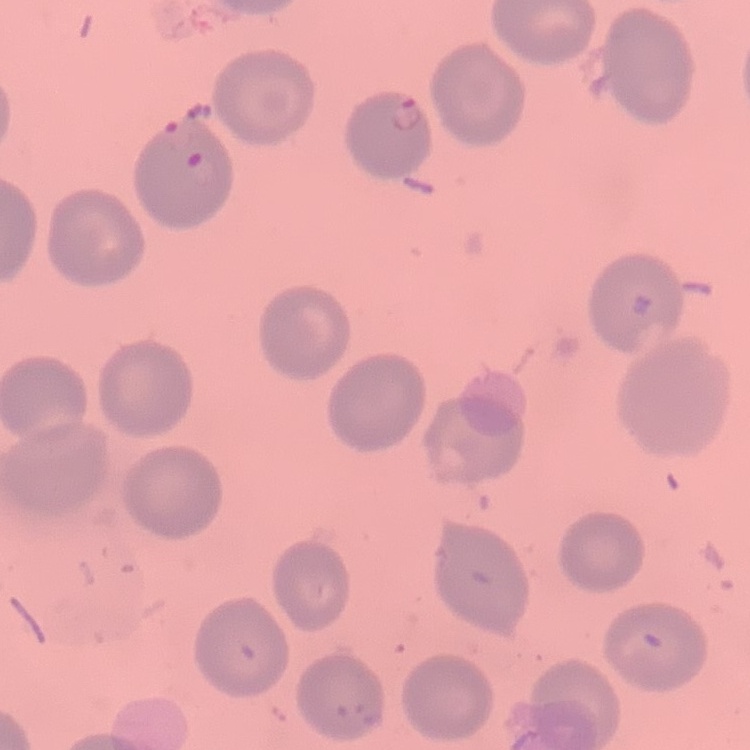 The erythrocytes exhibit no rouleaux formation. One tile cut from a larger photomicrograph. Thin peripheral smear. Stained with either Field's or Giemsa.